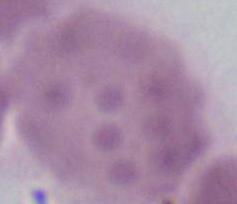
Summary:
  - Identification: red blood cell
  - Magnification: 1000x
  - Modality: photomicrograph